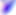

modality = photomicrograph
identification = Toxoplasma gondii
magnification = 400x